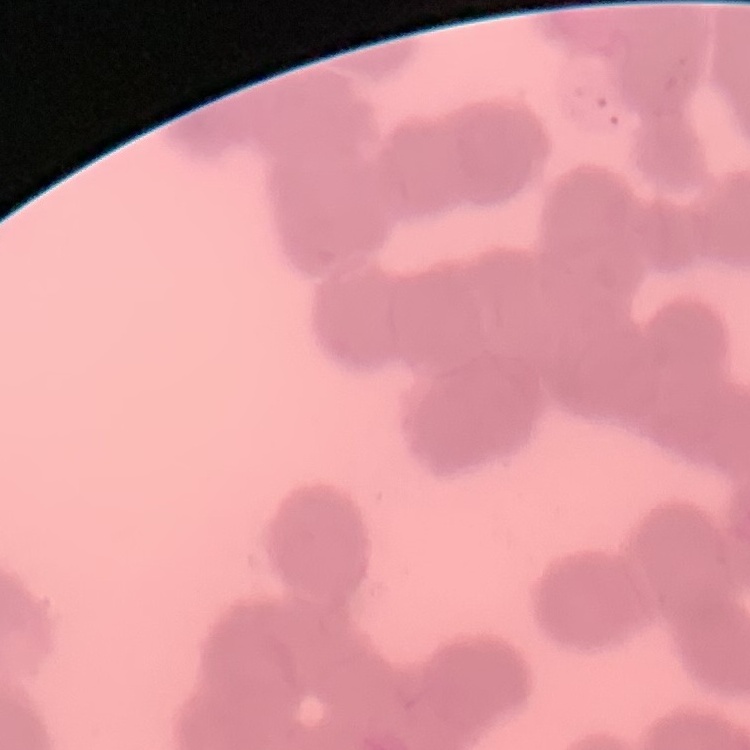

red blood cell morphology = rouleaux formation
image type = one tile cut from a larger photomicrograph
stain = Field's or Giemsa
preparation = thin blood smear